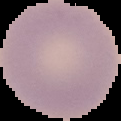

Summary:
  - Preparation: thin blood smear
  - Image size: 121×121 pixels
  - Image type: cell region segmented out of the field of view; surrounding area masked to black
  - Malaria status: uninfected